Report the malaria status of this cell.
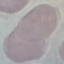
Uninfected.

Thin blood smear. Cell patch, automatically extracted from a larger field of view and resized to 64 × 64 pixels. Photographed with a smartphone camera at the microscope eyepiece. Giemsa-stained preparation.